Report the malaria status of this cell.
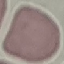
It is uninfected.

preparation = thin blood smear
capture = smartphone through the microscope eyepiece
image type = cell patch, automatically extracted from a larger field of view and resized to 64 × 64 pixels
stain = Giemsa